Identify the parasite.
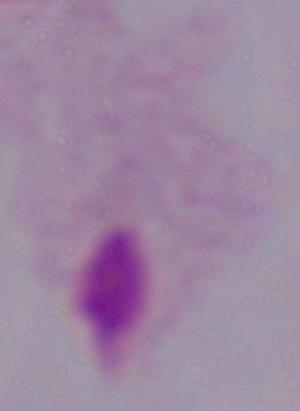
A trichomonad.

Micrograph. 1000x magnification.